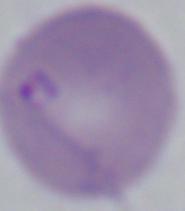

modality = photomicrograph
identification = Babesia
magnification = 1000x